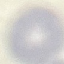 Result: no malaria parasites seen. Thin blood smear. Photographed with a smartphone camera at the microscope eyepiece. Cell patch, automatically extracted from a larger field of view and resized to 64 × 64 pixels. Giemsa stain.